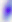
Summary:
  - Identification: Toxoplasma gondii
  - Magnification: 400x
  - Modality: photomicrograph